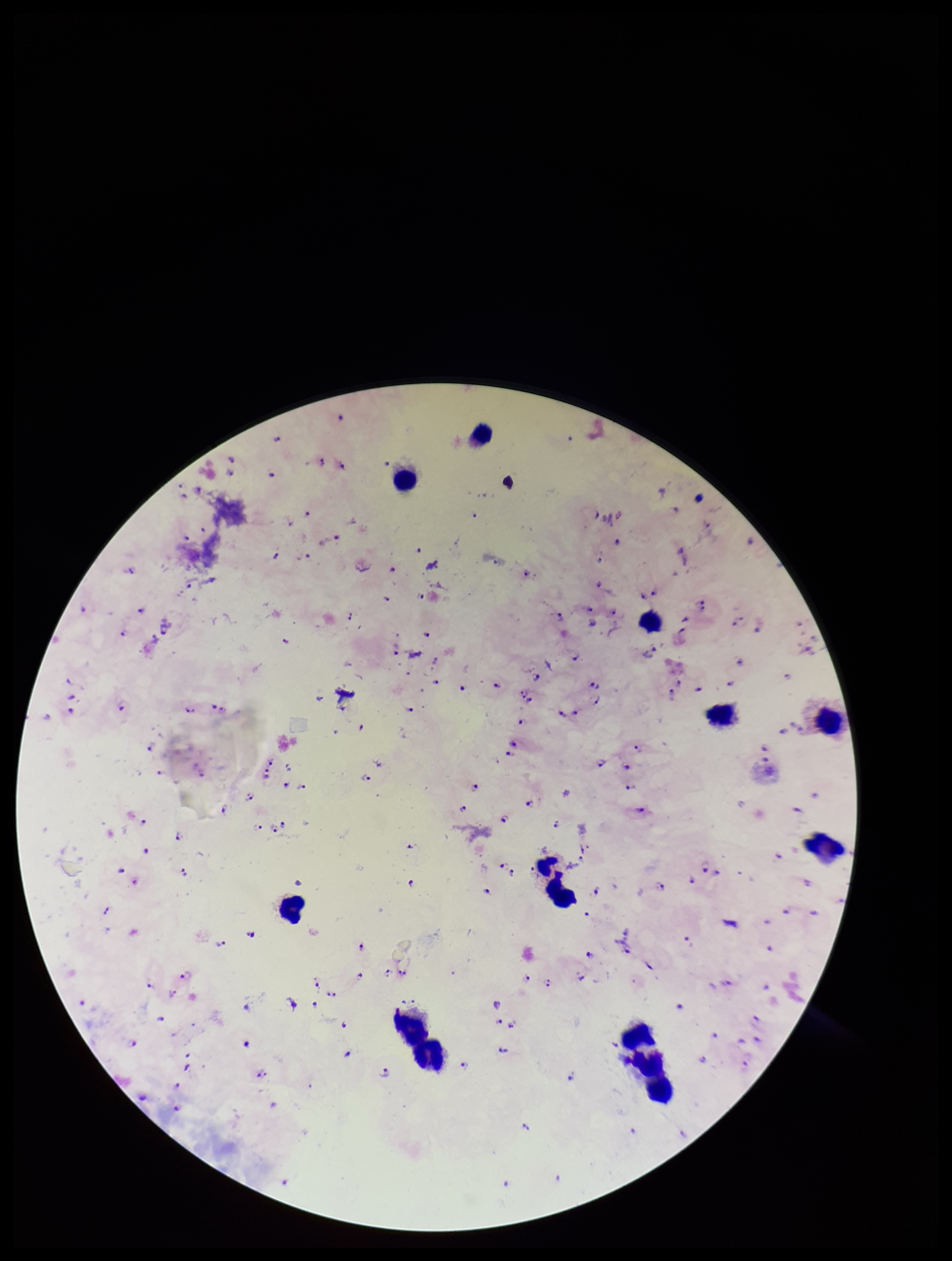
Plasmodium parasites: identified. One field from this slide. Patient malaria status: infected. Preparation: thick smear. Smartphone photograph taken through the eyepiece of a microscope. Species reported for this patient: Plasmodium falciparum. Giemsa stain. Image is 952×1261 pixels. Parasite count: 99. Leukocyte count: 12.